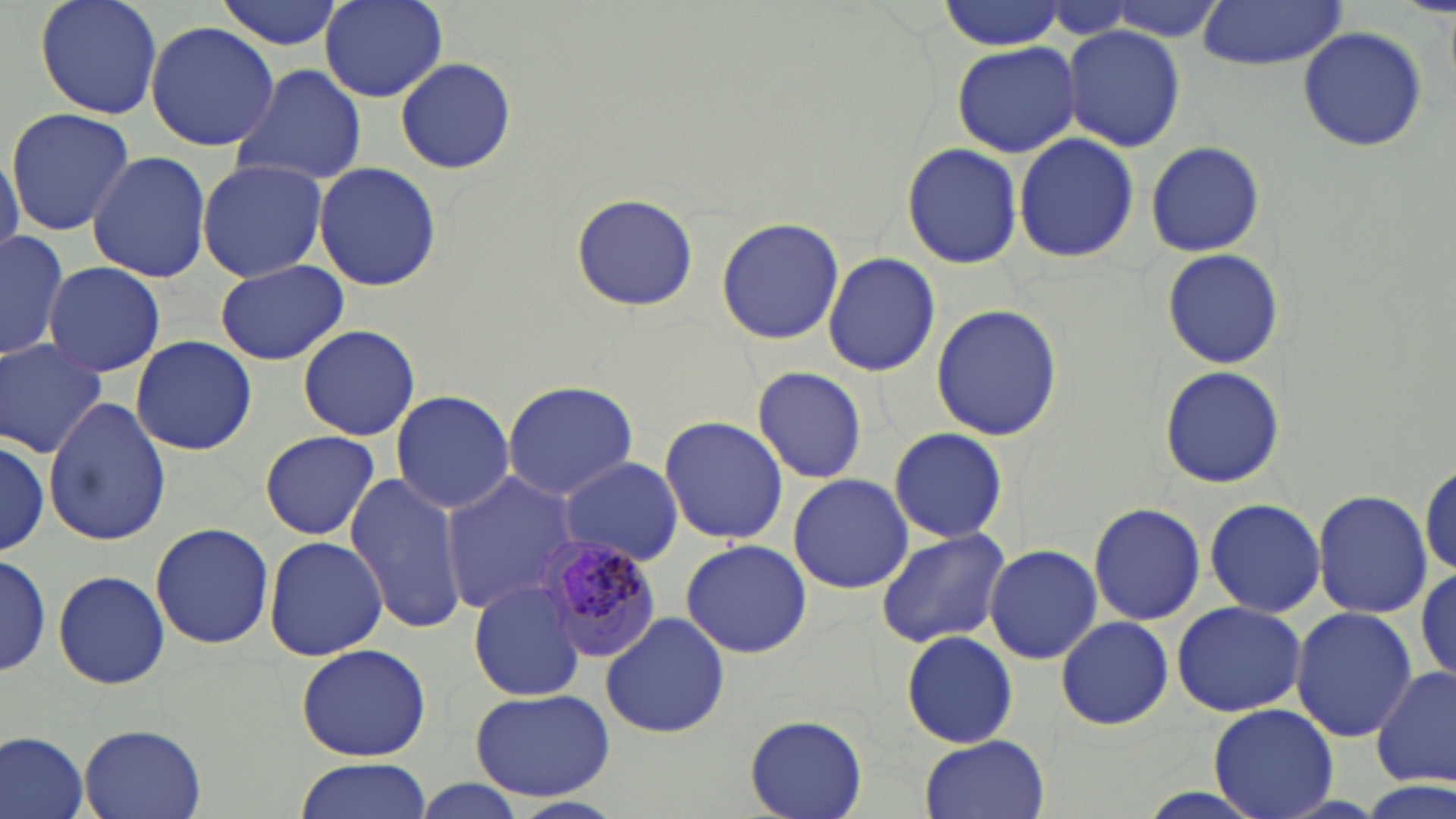
Approximate bounding boxes as named x1/y1/x2/y2 corners in pixels. Uninfected red blood cell locations: (x1=34, y1=0, x2=163, y2=119), (x1=214, y1=0, x2=344, y2=51), (x1=321, y1=1, x2=446, y2=102), (x1=1192, y1=1, x2=1349, y2=71), (x1=936, y1=3, x2=1067, y2=50), (x1=144, y1=20, x2=279, y2=152), (x1=1062, y1=24, x2=1185, y2=152), (x1=1297, y1=25, x2=1427, y2=153), (x1=951, y1=40, x2=1081, y2=159), (x1=395, y1=58, x2=515, y2=174), (x1=230, y1=64, x2=368, y2=186), (x1=6, y1=106, x2=135, y2=234), (x1=1013, y1=133, x2=1138, y2=265), (x1=1143, y1=140, x2=1267, y2=257), (x1=900, y1=141, x2=1023, y2=269), (x1=0, y1=151, x2=22, y2=262), (x1=87, y1=151, x2=213, y2=284), (x1=196, y1=159, x2=329, y2=282), (x1=313, y1=162, x2=441, y2=292), (x1=568, y1=193, x2=699, y2=312), (x1=716, y1=216, x2=844, y2=345), (x1=0, y1=231, x2=70, y2=358), (x1=1162, y1=249, x2=1282, y2=369), (x1=823, y1=252, x2=941, y2=377), (x1=214, y1=259, x2=348, y2=367), (x1=42, y1=261, x2=165, y2=378), (x1=931, y1=304, x2=1063, y2=440), (x1=298, y1=323, x2=420, y2=441), (x1=130, y1=335, x2=256, y2=456), (x1=1, y1=337, x2=108, y2=458), (x1=1159, y1=365, x2=1284, y2=488), (x1=752, y1=366, x2=868, y2=485), (x1=501, y1=380, x2=638, y2=499), (x1=390, y1=388, x2=516, y2=514), (x1=43, y1=395, x2=173, y2=546), (x1=657, y1=415, x2=789, y2=544), (x1=887, y1=426, x2=1009, y2=543), (x1=260, y1=429, x2=379, y2=540), (x1=0, y1=433, x2=49, y2=559), (x1=557, y1=455, x2=684, y2=566), (x1=1418, y1=461, x2=1454, y2=581), (x1=442, y1=472, x2=588, y2=614), (x1=788, y1=473, x2=913, y2=594), (x1=345, y1=474, x2=473, y2=635), (x1=1314, y1=490, x2=1430, y2=618), (x1=1204, y1=497, x2=1325, y2=617), (x1=1087, y1=501, x2=1207, y2=626), (x1=151, y1=522, x2=273, y2=649), (x1=875, y1=527, x2=1009, y2=649), (x1=264, y1=534, x2=388, y2=660), (x1=680, y1=541, x2=811, y2=657), (x1=984, y1=543, x2=1102, y2=665), (x1=0, y1=551, x2=50, y2=681), (x1=0, y1=552, x2=52, y2=676), (x1=1415, y1=563, x2=1455, y2=685), (x1=51, y1=571, x2=171, y2=690), (x1=467, y1=580, x2=586, y2=703), (x1=1171, y1=600, x2=1307, y2=717), (x1=1291, y1=607, x2=1419, y2=741), (x1=599, y1=610, x2=730, y2=739), (x1=1055, y1=614, x2=1174, y2=731), (x1=901, y1=630, x2=1019, y2=748), (x1=294, y1=641, x2=434, y2=762), (x1=1371, y1=663, x2=1455, y2=789), (x1=467, y1=687, x2=616, y2=802), (x1=1208, y1=702, x2=1339, y2=819), (x1=744, y1=714, x2=867, y2=818), (x1=78, y1=725, x2=207, y2=818), (x1=1, y1=731, x2=90, y2=819), (x1=918, y1=735, x2=1049, y2=819), (x1=292, y1=757, x2=434, y2=819), (x1=408, y1=782, x2=528, y2=819). Plasmodium malariae-infected red blood cell locations: (x1=541, y1=537, x2=661, y2=662). Slide-level diagnosis: Plasmodium malariae. May-Grünwald-Giemsa stain. One field of a larger specimen. Optical microscopy. Thin blood film. Captured at 1000x magnification. Image is 1456×819 pixels.